Describe the morphology of the erythrocytes.
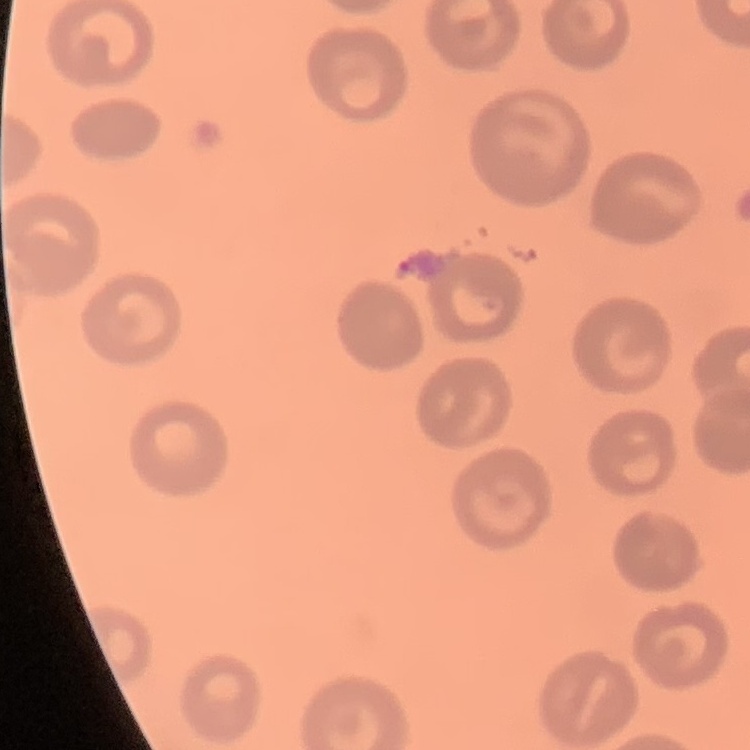
No rouleaux formation.

Summary:
  - Preparation: thin peripheral smear
  - Image type: square crop of a larger photomicrograph
  - Stain: Field's or Giemsa